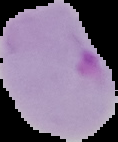

image size = 118×142 pixels
image type = segmented cell region with the area outside set to black
preparation = thin blood film
malaria status = parasitized